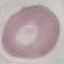

malaria_status: uninfected
preparation: thin blood film
stain: Giemsa
image_type: cell patch, automatically extracted from a larger field of view and resized to 64 × 64 pixels
capture: smartphone through the microscope eyepiece